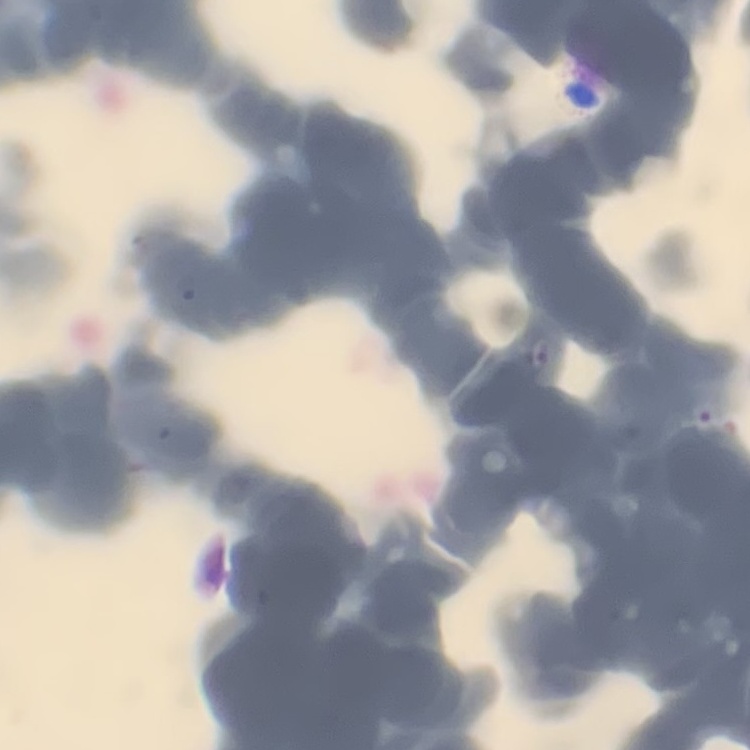
The erythrocytes exhibit rouleaux formation. Thin blood smear. One tile cut from a larger photomicrograph. Field's or Giemsa stain.